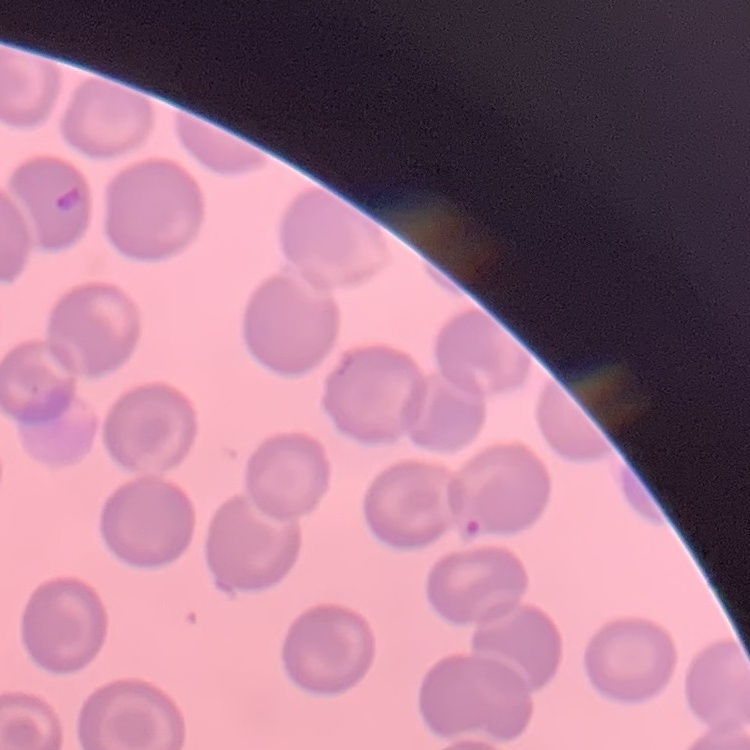

erythrocyte_morphology: no rouleaux formation
stain: Field's or Giemsa
image_type: square crop of a larger photomicrograph
preparation: thin blood film